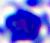
magnification = 400x
identification = leukocyte
modality = micrograph